Report the malaria status of this cell.
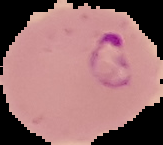
It is parasitized.

From a thin blood film. Image is 163×145 pixels. Segmented cell region on a black background.